Assess this cell for malaria.
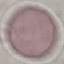

It is uninfected.

image type = cell patch, automatically extracted from a larger field of view and resized to 64 × 64 pixels
stain = Giemsa
preparation = thin blood smear
capture = smartphone through the microscope eyepiece